Report the malaria status of this cell.
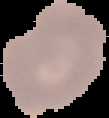

Uninfected.

Summary:
  - Preparation: thin blood smear
  - Image size: 109×118 pixels
  - Image type: segmented cell region on a black background